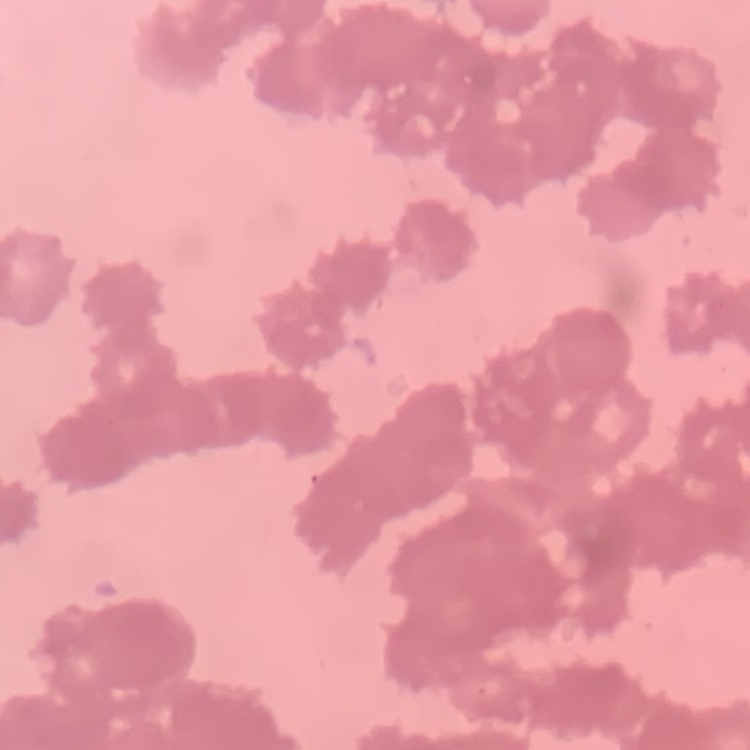

erythrocyte morphology = rouleaux formation
image type = square crop of a larger photomicrograph
preparation = thin blood film
stain = Field's or Giemsa